State which parasite is depicted.
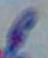

This is Toxoplasma gondii.

modality = photomicrograph
magnification = 1000x